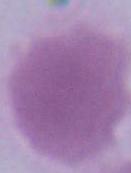
magnification = 1000x
identification = erythrocyte
modality = micrograph